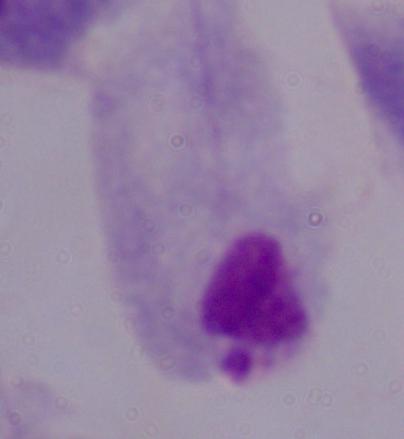
Summary:
  - Identification: trichomonad
  - Modality: photomicrograph
  - Magnification: 1000x